Report the malaria status.
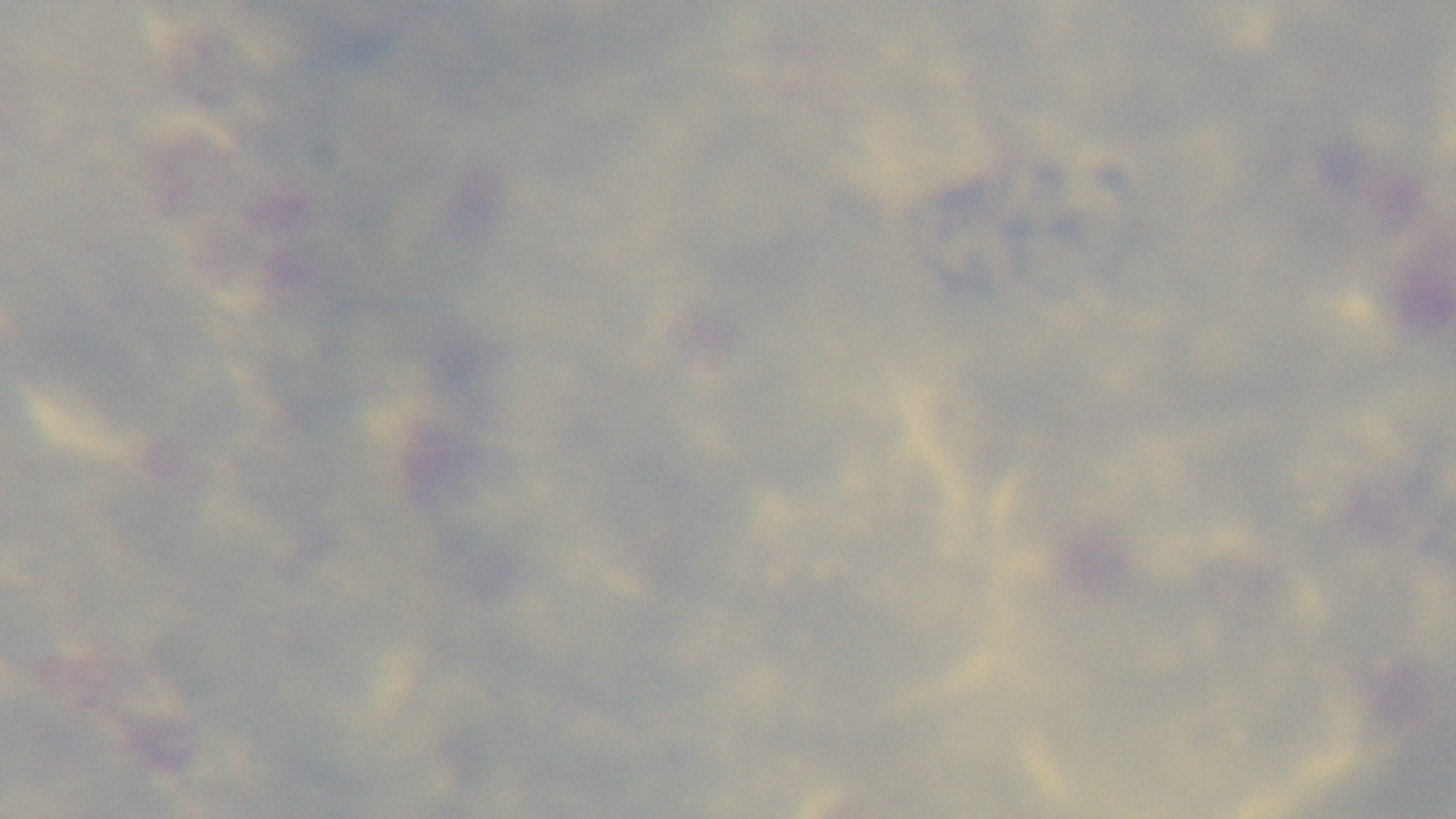
It is uninfected.

Summary:
  - Modality: light microscopy
  - Field of view: single
  - Objective: 100x oil immersion
  - Preparation: thick
  - Stain: Giemsa
  - Capture: mounted 4K digital camera